State the preparation type.
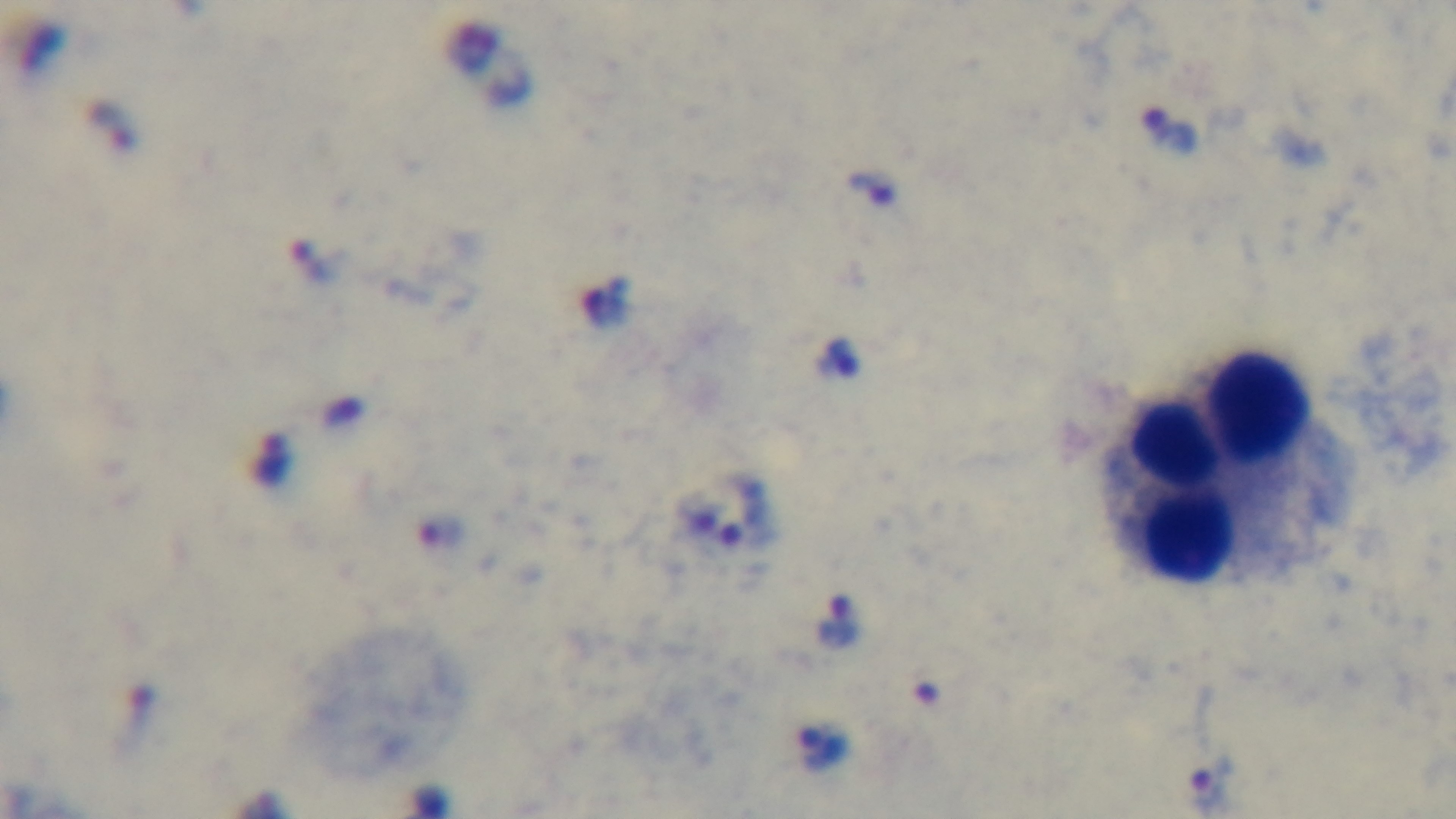
A thick smear.

capture: mounted 4K digital camera
stain: Giemsa
objective: 100x oil immersion
modality: light microscopy
field_of_view: single
malaria_status: infected